Outline each blood parasite and name the species.
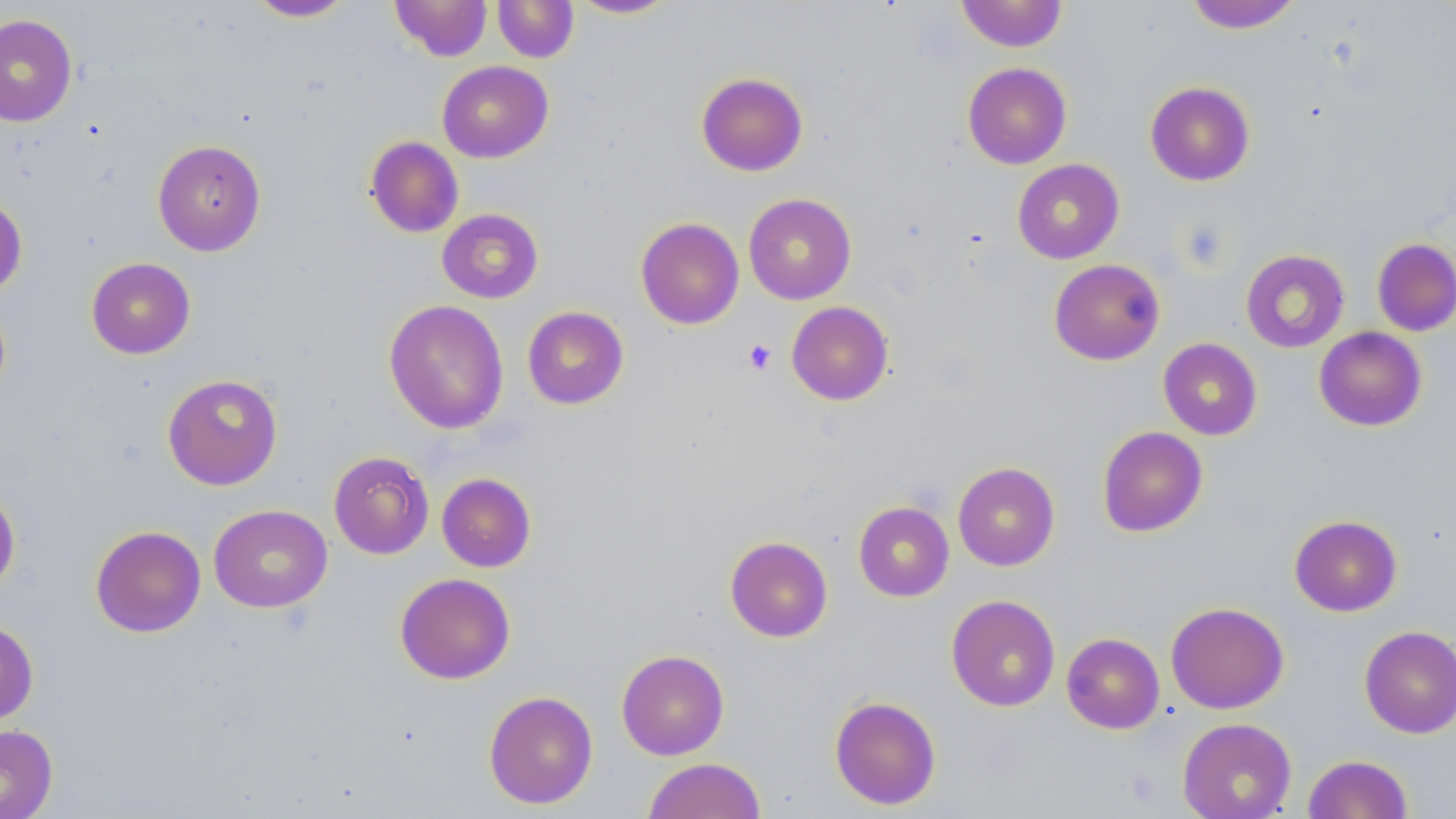
No blood parasites seen.

Approximate bounding boxes as (x1, y1, x2, y2) in pixels. Uninfected red blood cell locations: (245, 0, 357, 22), (390, 0, 492, 61), (492, 0, 579, 63), (568, 0, 680, 19), (956, 0, 1068, 52), (1185, 1, 1302, 33), (0, 13, 77, 126), (437, 60, 553, 163), (962, 62, 1072, 169), (696, 71, 808, 176), (1145, 81, 1255, 186), (365, 136, 464, 237), (152, 139, 266, 256), (1011, 159, 1124, 264), (743, 193, 857, 305), (0, 194, 28, 299), (436, 208, 544, 304), (635, 217, 744, 329), (1372, 237, 1456, 336), (1241, 249, 1350, 353), (86, 257, 195, 359), (1049, 258, 1165, 365), (384, 299, 509, 435), (786, 301, 894, 405), (522, 306, 629, 409), (1314, 326, 1427, 431), (1158, 338, 1262, 440), (162, 373, 283, 490), (1097, 426, 1208, 537), (329, 451, 434, 559), (953, 462, 1060, 571), (437, 472, 536, 572), (0, 486, 20, 595), (853, 501, 954, 601), (208, 504, 332, 613), (1289, 514, 1402, 616), (90, 525, 206, 637), (724, 535, 833, 642), (395, 572, 515, 684), (946, 594, 1060, 711), (1165, 602, 1289, 714), (0, 619, 38, 724), (1359, 625, 1456, 738), (1061, 632, 1164, 734), (616, 649, 729, 760), (483, 690, 598, 809), (829, 695, 941, 810), (1177, 717, 1297, 819), (0, 724, 57, 819), (1302, 754, 1414, 818), (642, 757, 766, 819). Platelet locations: (742, 338, 777, 375). Slide-level diagnosis: no evidence of blood parasites. 1000x magnification. Thin blood film. Image is 1456×819 pixels. Light microscopy. May-Grünwald-Giemsa stain. Single field of view.